Identify the parasite.
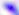

Toxoplasma gondii.

Captured at 400x magnification. Micrograph.